Comment on the morphology of the erythrocytes.
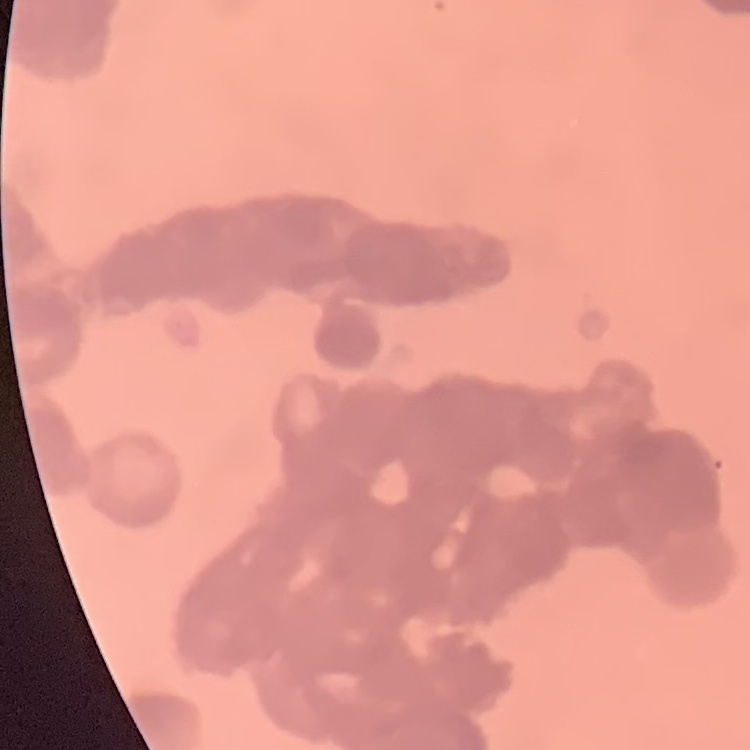
Rouleaux formation.

{
  "preparation": "thin blood smear",
  "stain": "Field's or Giemsa",
  "image_type": "one tile cut from a larger photomicrograph"
}